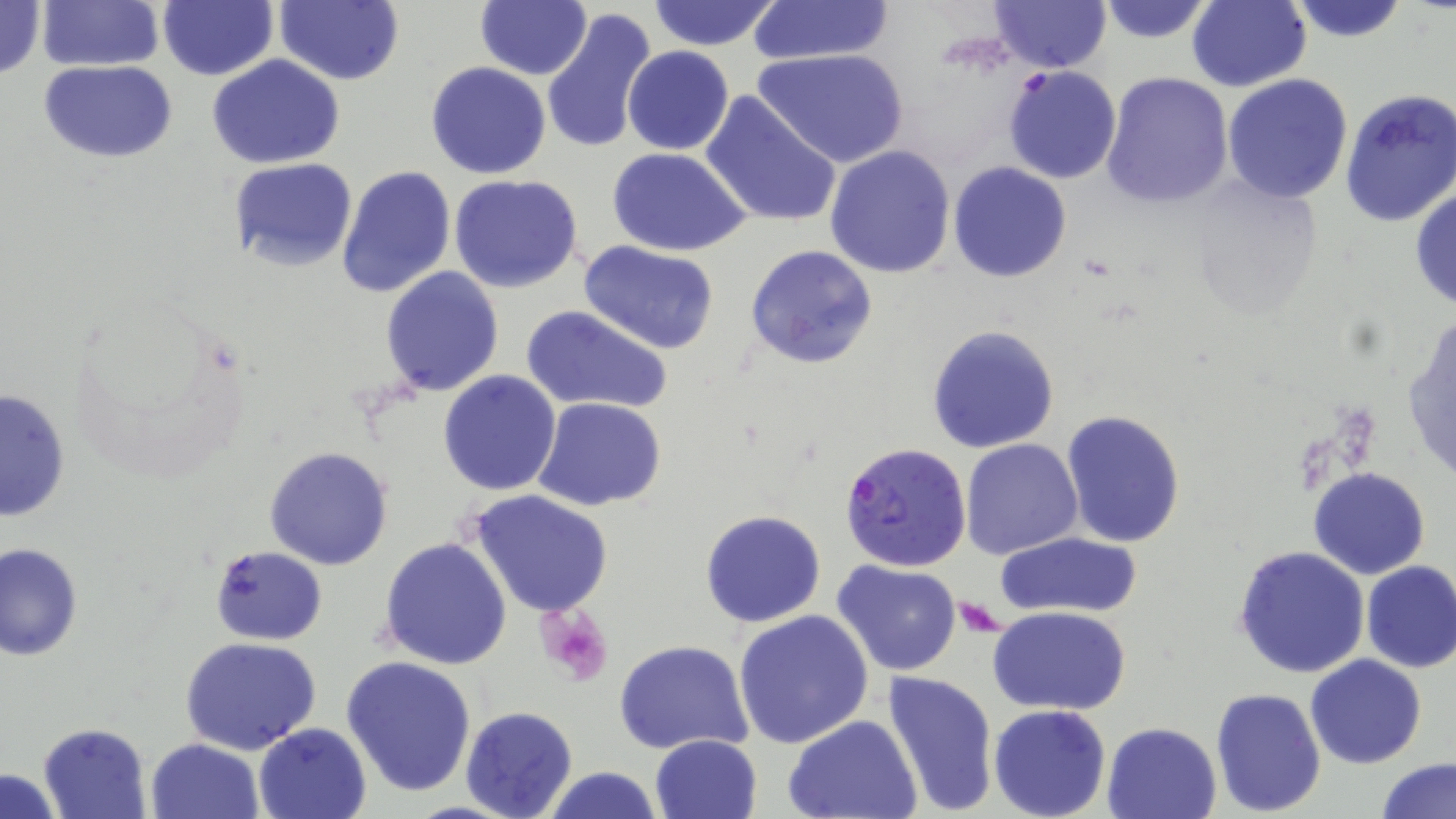

slide-level diagnosis = Plasmodium falciparum
image size = 1456×819 pixels
platelet locations = approximate bounding boxes as (x1, y1, x2, y2) in pixels: (954, 599, 1004, 636), (534, 602, 614, 686)
field of view = single
preparation = thin blood smear
uninfected red blood cell locations = approximate bounding boxes as (x1, y1, x2, y2) in pixels: (158, 0, 277, 81), (275, 0, 403, 85), (747, 0, 898, 66), (988, 0, 1111, 72), (1091, 0, 1218, 45), (1186, 0, 1310, 92), (1282, 0, 1415, 43), (0, 1, 47, 80), (37, 1, 166, 72), (646, 1, 784, 50), (474, 2, 593, 80), (542, 7, 657, 154), (623, 45, 734, 156), (755, 48, 909, 168), (208, 54, 345, 168), (39, 60, 178, 163), (426, 61, 551, 178), (1003, 66, 1123, 184), (1100, 72, 1235, 210), (1222, 74, 1354, 205), (1339, 87, 1456, 228), (699, 90, 844, 229), (824, 145, 956, 278), (609, 148, 751, 256), (228, 158, 360, 275), (949, 163, 1071, 283), (335, 165, 456, 300), (1185, 171, 1328, 314), (449, 174, 585, 293), (1409, 183, 1456, 311), (577, 239, 721, 353), (745, 244, 878, 369), (380, 267, 504, 396), (523, 306, 671, 416), (1403, 311, 1456, 486), (927, 323, 1059, 452), (438, 371, 562, 495), (0, 386, 71, 523), (535, 398, 666, 512), (1060, 409, 1185, 547), (960, 437, 1083, 559), (264, 446, 393, 570), (1309, 467, 1430, 579), (467, 489, 618, 617), (698, 510, 827, 628), (993, 529, 1144, 620), (378, 537, 512, 669), (0, 542, 83, 661), (210, 544, 327, 646), (1232, 547, 1372, 680), (832, 560, 964, 676), (1360, 560, 1456, 673), (990, 605, 1132, 715), (732, 609, 874, 748), (179, 637, 322, 755), (613, 639, 754, 753), (342, 654, 478, 796), (1305, 655, 1428, 769), (882, 670, 1000, 815), (1211, 687, 1326, 813), (989, 703, 1111, 819), (460, 704, 577, 818), (784, 716, 921, 819), (36, 721, 152, 818), (253, 721, 374, 818), (1100, 721, 1221, 819), (650, 734, 762, 819), (145, 737, 264, 819), (1375, 756, 1456, 818), (538, 766, 663, 819), (0, 770, 65, 818)
modality = optical microscopy
Plasmodium falciparum-infected red blood cell locations = approximate bounding boxes as (x1, y1, x2, y2) in pixels: (838, 443, 971, 571)
stain = May-Grünwald-Giemsa
magnification = 1000x